Describe the morphology of the erythrocytes.
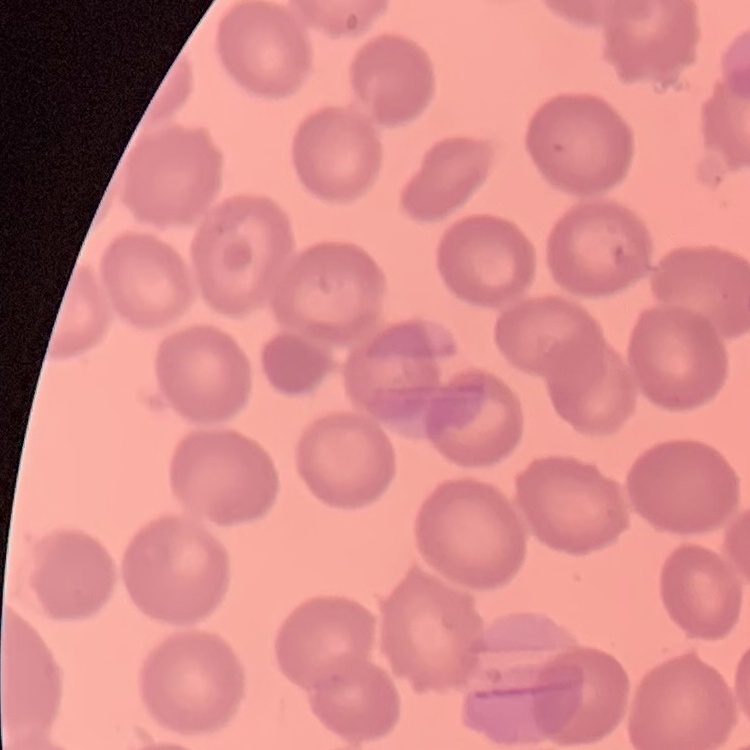
They show no rouleaux formation.

{
  "preparation": "thin blood smear",
  "stain": "Field's or Giemsa",
  "image_type": "square crop of a larger photomicrograph"
}